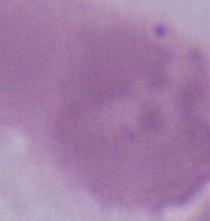 1000x magnification. Micrograph. A red blood cell is seen.